Give the preparation type.
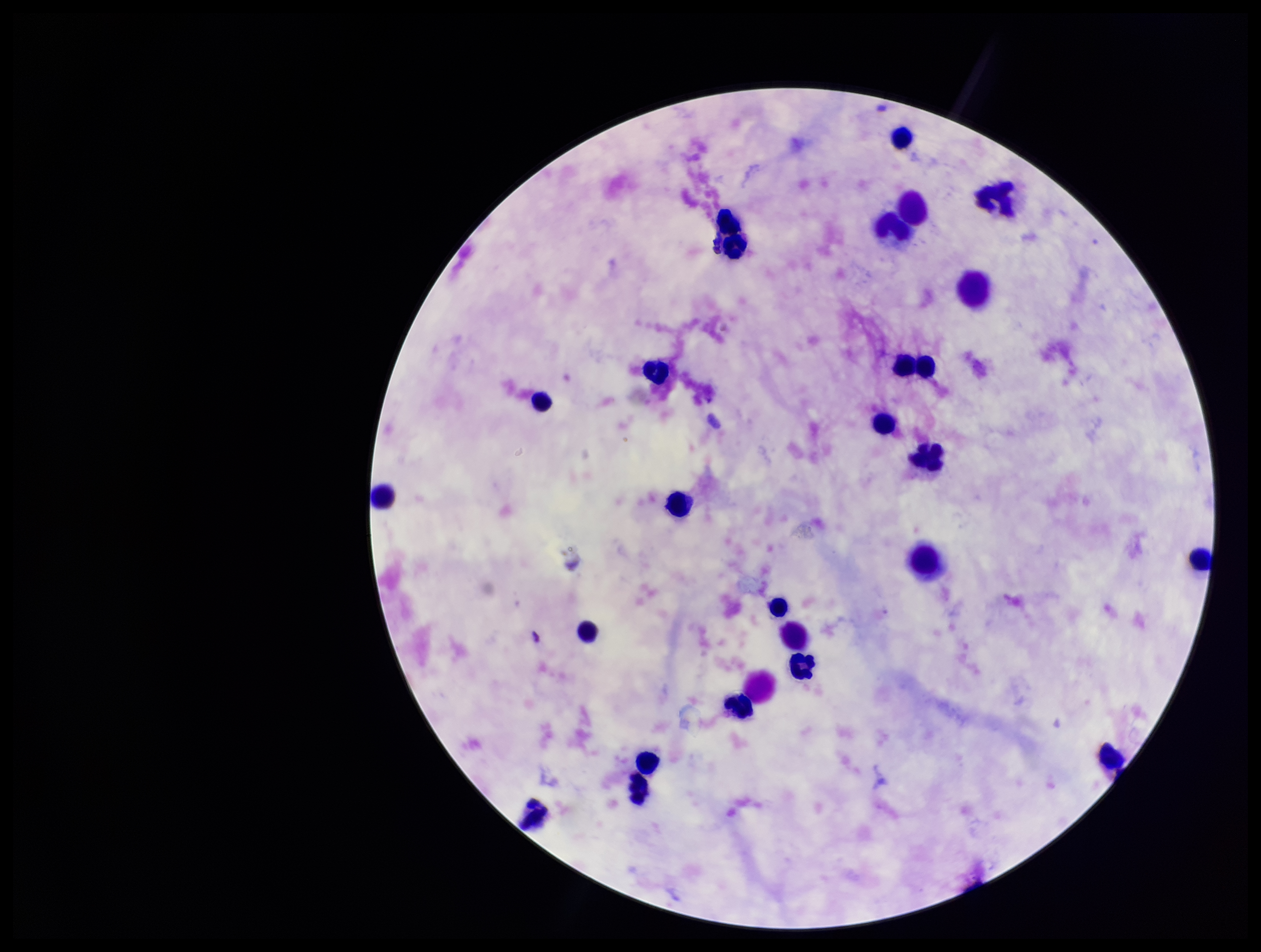
Thick.

Giemsa stain. Photographed through the microscope eyepiece with a smartphone camera. Leukocyte count: 24. Parasite count: 0. Image is 1261×952 pixels. One field from this slide. Patient malaria status: negative. Plasmodium parasites: none detected.